State the blood parasite species.
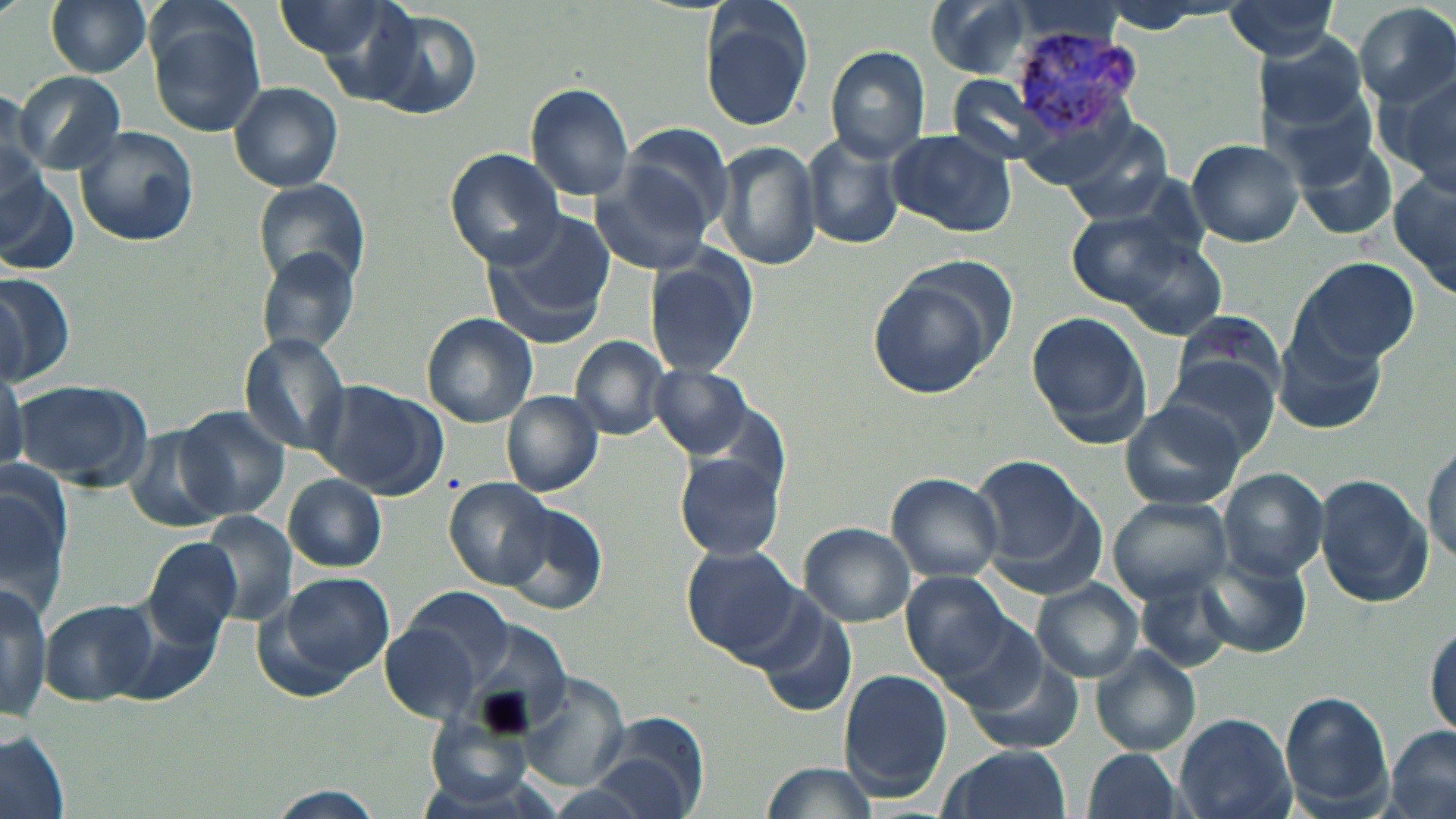

Plasmodium vivax.

Approximate bounding boxes as [x1, y1, x2, y2] in pixels. Plasmodium vivax-infected red blood cell locations: [1007, 22, 1143, 140]. Uninfected red blood cell locations: [274, 0, 397, 61], [923, 0, 1041, 78], [45, 1, 153, 78], [697, 2, 812, 131], [1220, 3, 1343, 63], [1353, 3, 1456, 108], [360, 7, 484, 120], [148, 12, 269, 140], [1253, 30, 1373, 134], [825, 45, 931, 164], [1379, 69, 1456, 197], [12, 72, 126, 174], [524, 81, 635, 203], [229, 82, 343, 192], [1267, 87, 1378, 190], [1060, 119, 1171, 223], [615, 123, 735, 235], [73, 125, 200, 248], [884, 129, 1016, 238], [803, 133, 905, 252], [1185, 137, 1305, 247], [717, 139, 821, 271], [1295, 142, 1400, 240], [444, 149, 567, 268], [590, 162, 716, 275], [0, 170, 79, 275], [1389, 172, 1456, 299], [255, 180, 370, 295], [1066, 206, 1201, 315], [483, 215, 614, 346], [1108, 233, 1229, 341], [255, 249, 362, 358], [645, 252, 756, 378], [1288, 256, 1421, 367], [867, 265, 1006, 399], [0, 271, 75, 388], [1026, 310, 1152, 447], [1172, 312, 1284, 406], [421, 314, 538, 428], [1275, 328, 1390, 433], [240, 333, 353, 455], [570, 334, 671, 439], [1159, 358, 1279, 463], [0, 363, 27, 475], [651, 364, 753, 458], [11, 379, 152, 491], [315, 381, 445, 498], [502, 390, 603, 497], [1118, 398, 1246, 512], [176, 405, 291, 521], [121, 425, 231, 535], [1423, 441, 1455, 571], [675, 453, 786, 563], [968, 454, 1103, 593], [2, 466, 70, 609], [1219, 468, 1330, 580], [885, 472, 1004, 583], [283, 473, 387, 573], [1315, 473, 1432, 609], [445, 478, 553, 588], [1108, 496, 1232, 603], [499, 501, 607, 616], [201, 511, 297, 625], [799, 522, 916, 627], [143, 537, 243, 647], [680, 545, 808, 666], [1196, 552, 1310, 658], [901, 569, 1018, 684], [279, 572, 394, 679], [1032, 580, 1143, 682], [1138, 581, 1234, 672], [0, 582, 51, 720], [397, 586, 519, 691], [42, 600, 155, 706], [753, 600, 859, 719], [917, 604, 1046, 714], [1425, 616, 1456, 739], [379, 619, 482, 725], [1092, 648, 1201, 756], [965, 657, 1085, 756], [839, 668, 953, 796], [512, 673, 631, 792], [1279, 690, 1390, 814], [583, 710, 709, 819], [1172, 712, 1296, 819], [425, 715, 540, 810], [1384, 727, 1455, 819], [0, 735, 71, 819], [938, 745, 1075, 819], [1080, 748, 1184, 819], [758, 762, 880, 818], [256, 789, 391, 819]. Captured at 1000x magnification. Thin blood smear. Single field of view. Image is 1456×819 pixels. Light microscopy. May-Grünwald-Giemsa stain.